Assess this cell for malaria.
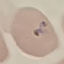

It is uninfected.

{
  "stain": "Giemsa",
  "capture": "smartphone camera at the microscope eyepiece",
  "preparation": "thin smear",
  "image_type": "cell patch, automatically extracted from a larger field of view and resized to 64 × 64 pixels"
}